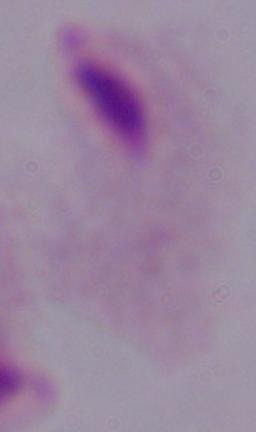
Summary:
  - Magnification: 1000x
  - Identification: trichomonad
  - Modality: photomicrograph